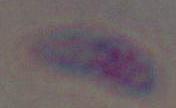
magnification = 1000x
identification = Toxoplasma gondii
modality = photomicrograph